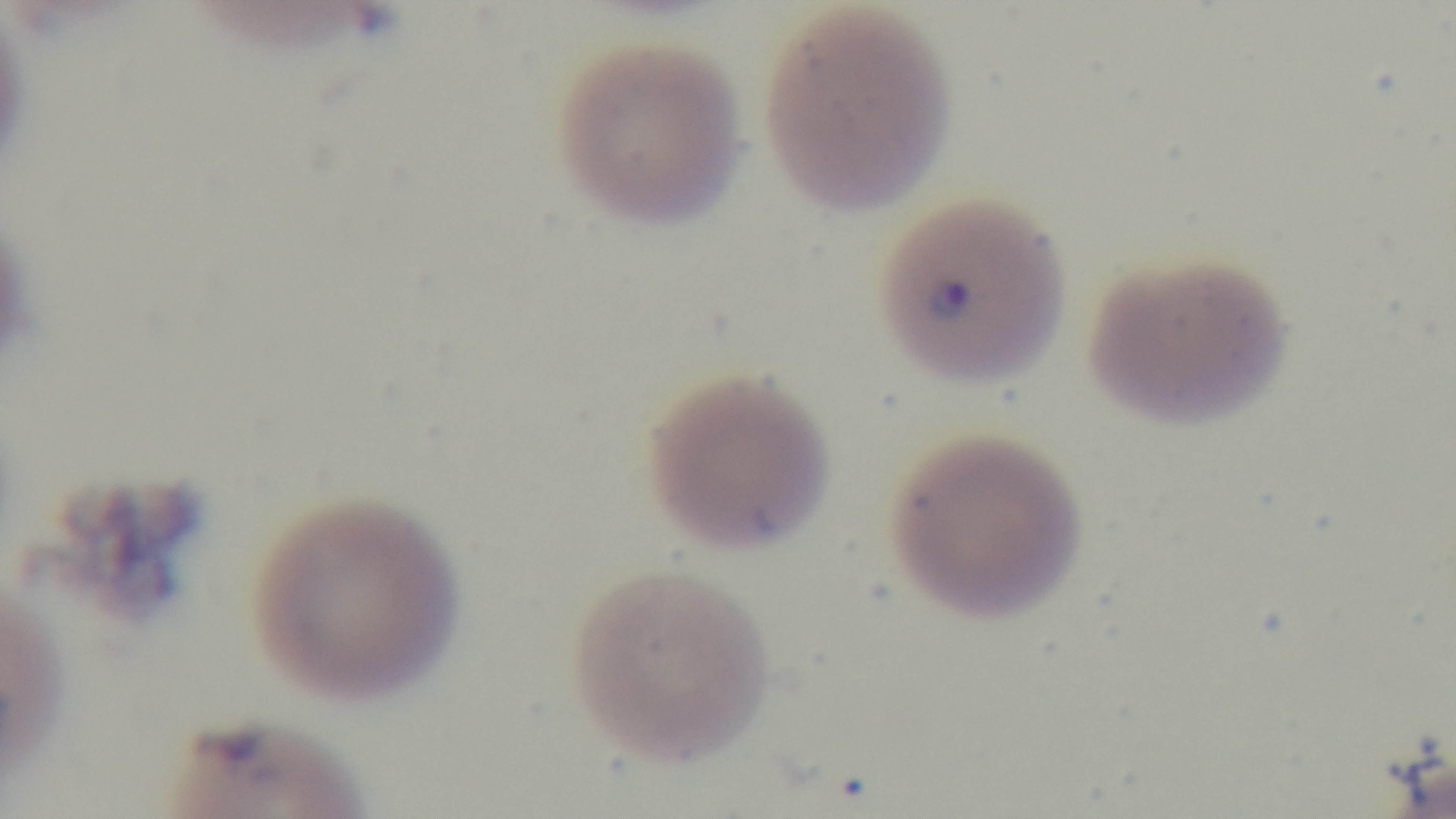
objective = 100x oil immersion
field of view = one from the slide
malaria status = positive
stain = Giemsa
preparation = thin smear
capture = mounted 4K digital camera
modality = light microscopy